Identify the parasite.
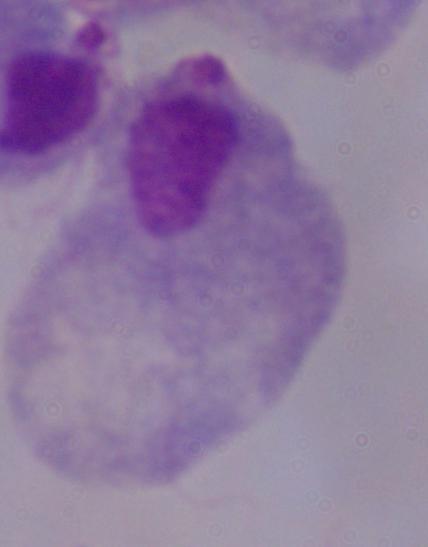

A trichomonad.

Photomicrograph. Captured at 1000x magnification.